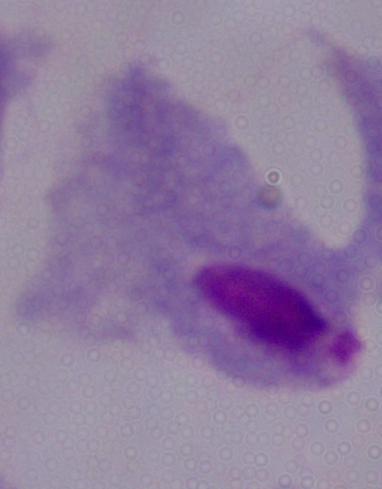 A trichomonad is seen. Photomicrograph. Captured at 1000x magnification.